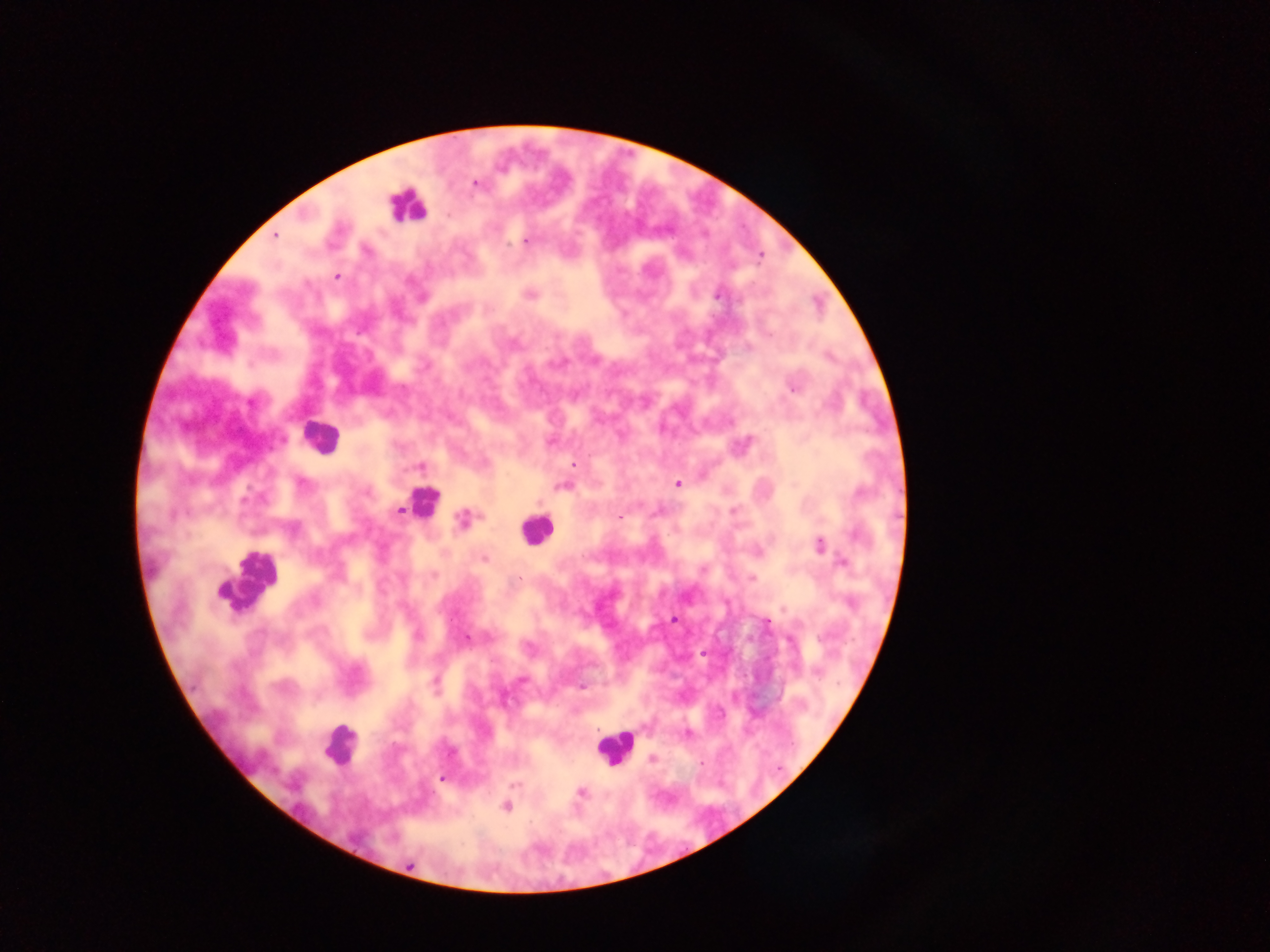 Approximate centers as {x, y} in pixels. Leukocyte locations: {405, 206}, {320, 436}, {424, 502}, {537, 530}, {250, 582}, {338, 745}, {614, 746}. Malaria parasite locations: {475, 183}, {447, 215}, {275, 236}, {526, 242}, {760, 257}, {337, 277}, {530, 294}, {717, 295}, {421, 298}, {792, 388}, {252, 402}, {550, 442}, {574, 465}, {419, 467}, {302, 484}, {677, 484}, {563, 486}, {367, 493}, {861, 493}, {246, 499}, {399, 511}, {620, 517}, {461, 519}, {857, 535}, {819, 545}, {484, 559}, {842, 562}, {520, 578}, {752, 579}, {674, 620}, {766, 622}, {417, 635}, {467, 637}, {521, 679}, {435, 683}, {581, 687}, {687, 734}, {653, 758}, {442, 778}, {514, 784}, {581, 792}, {506, 807}, {408, 865}. Image is 1270×952 pixels. Sample from Ghana. Thick blood smear. One field of view. Mobile-phone photograph taken through the microscope.